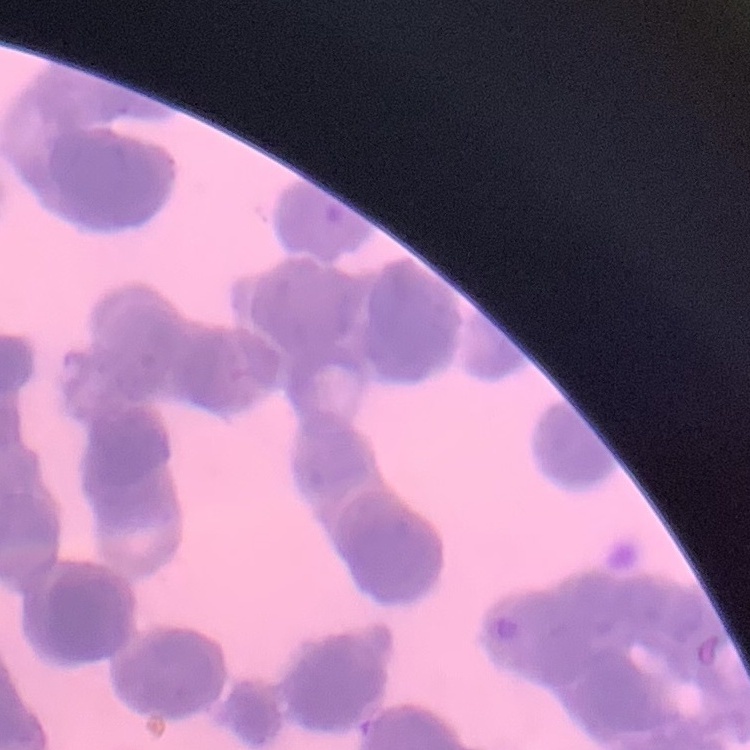
The erythrocytes show rouleaux formation. Thin peripheral smear. Stained with either Field's or Giemsa. Square crop of a larger photomicrograph.